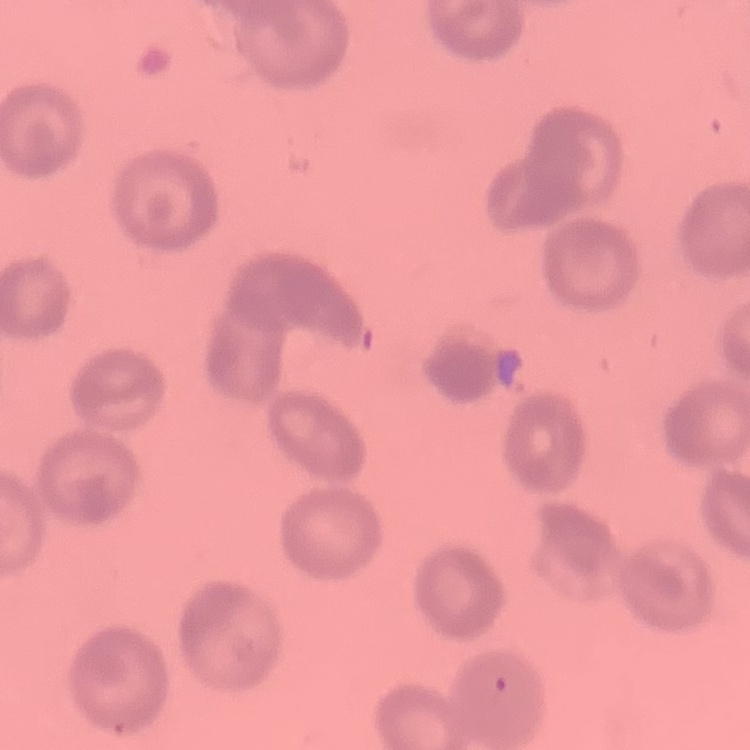
Summary:
  - Erythrocyte morphology: rouleaux formation
  - Image type: square crop of a larger photomicrograph
  - Stain: Field's or Giemsa
  - Preparation: thin blood smear